Assess this cell for malaria.
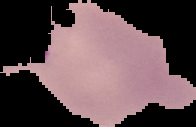

Parasitized.

image size = 196×127 pixels
image type = segmented cell region with the area outside set to black
preparation = thin blood film